Assess the morphology of the red blood cells.
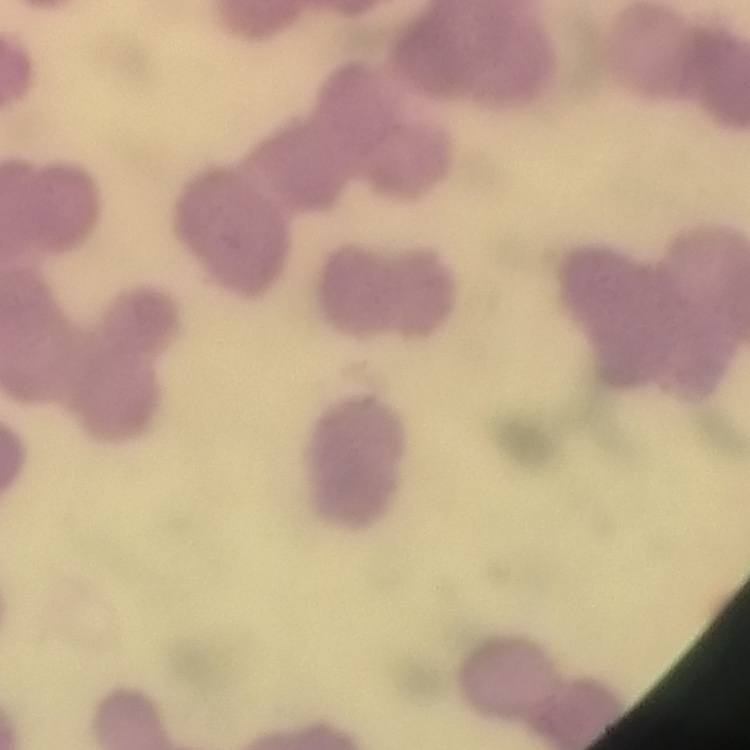
Rouleaux formation.

Summary:
  - Preparation: thin blood film
  - Stain: Field's or Giemsa
  - Image type: one tile cut from a larger photomicrograph